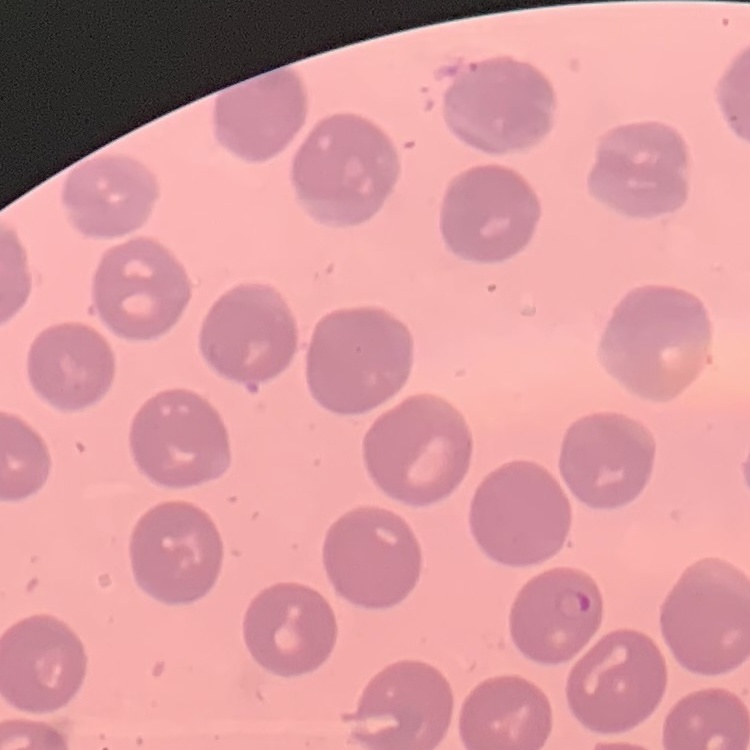

Summary:
  - Red blood cell morphology: no rouleaux formation
  - Preparation: thin peripheral smear
  - Image type: one tile cut from a larger photomicrograph
  - Stain: Field's or Giemsa